Assess this cell for malaria.
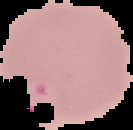

It is parasitized.

preparation = thin blood film
image size = 133×130 pixels
image type = segmented cell region with the area outside set to black